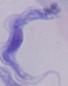
{
  "magnification": "1000x",
  "identification": "trypanosome",
  "modality": "micrograph"
}